Give the position of every Plasmodium parasite.
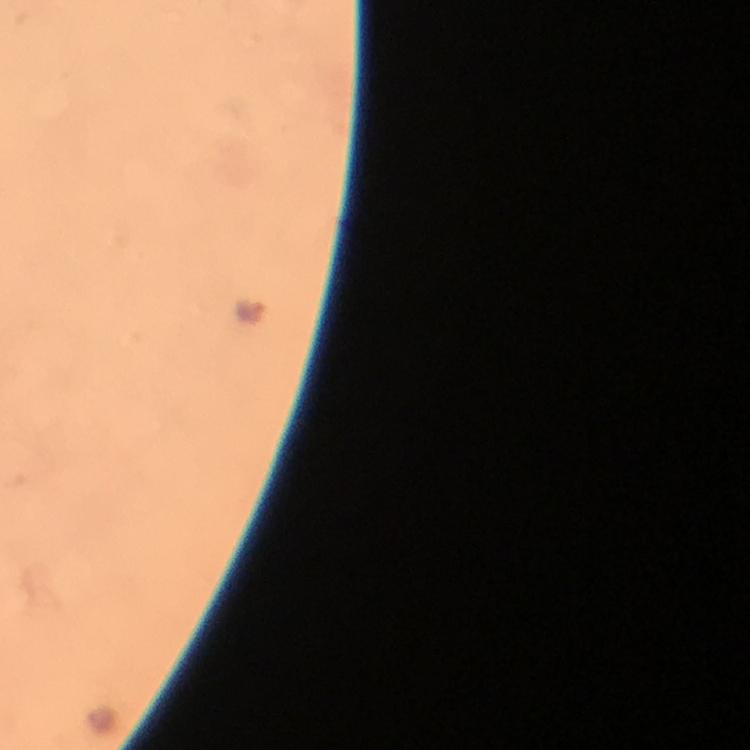
Approximate centers as (x, y) in pixels.
Plasmodium parasites: (250, 311).

preparation: thick smear
image_size: 750×750 pixels
capture: smartphone camera through the microscope
magnification: 100x
context: from a malaria diagnostic workup
stain: Giemsa
immersion_oil: used
cropped_from: a single field of view